Assess the morphology of the erythrocytes.
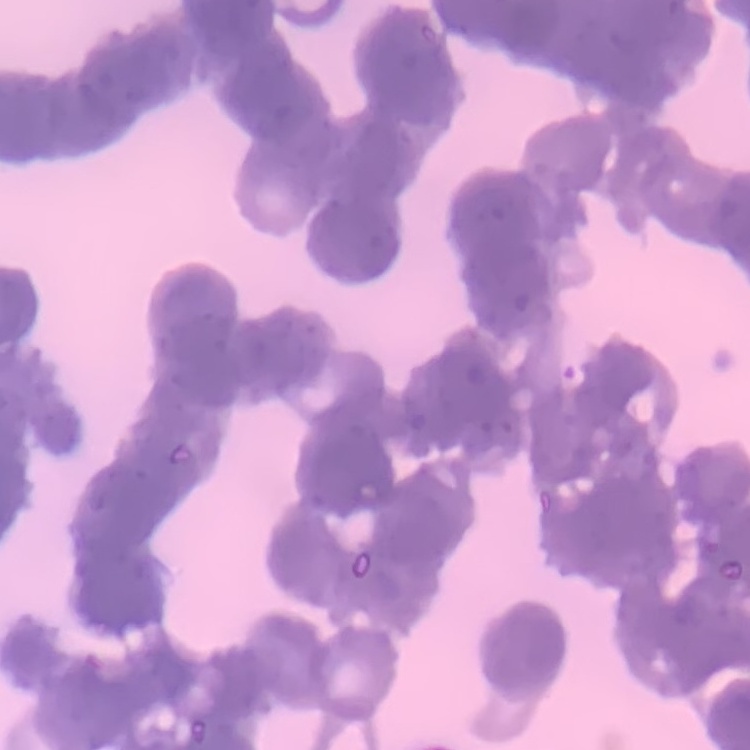
Rouleaux formation.

image type = one tile cut from a larger photomicrograph
preparation = thin peripheral smear
stain = Field's or Giemsa